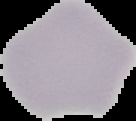 From a thin blood film. Image is 136×121 pixels. Segmented cell region on a black background. Malaria status: uninfected.